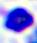

Micrograph. A leukocyte is seen. 400x magnification.